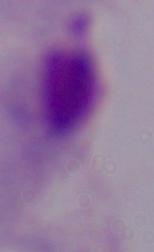
{
  "identification": "trichomonad",
  "magnification": "1000x",
  "modality": "photomicrograph"
}